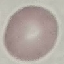

Summary:
  - Result: no malaria parasites detected
  - Image type: cell patch, automatically extracted from a larger field of view and resized to 64 × 64 pixels
  - Stain: Giemsa
  - Preparation: thin blood smear
  - Capture: smartphone camera at the microscope eyepiece